Locate and identify every blood parasite.
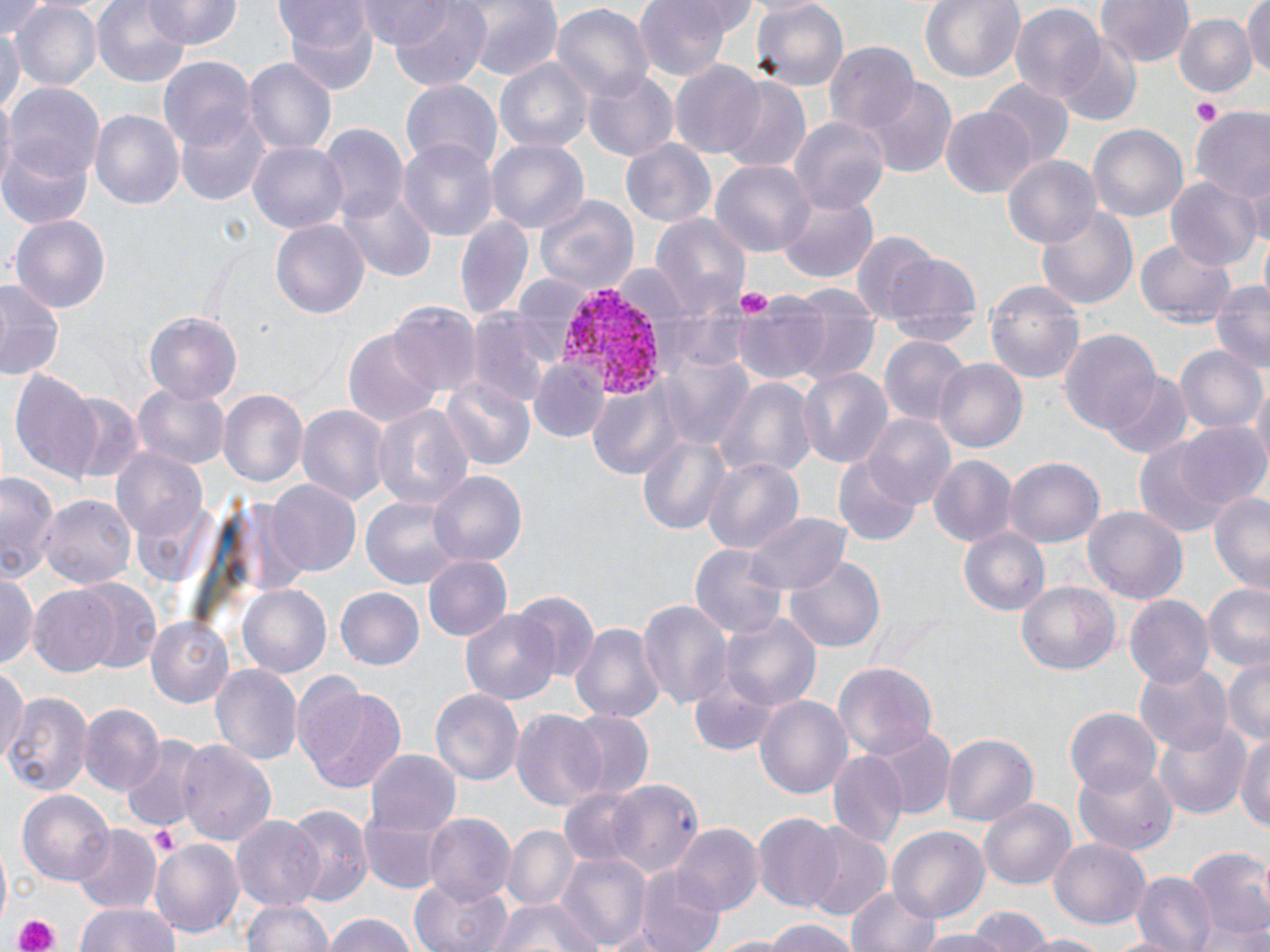

Approximate bounding boxes as (x1,y1)-(x2,y2) corner pairs in pixels.
Plasmodium vivax-infected red blood cells: (559,284)-(669,401).
No Plasmodium falciparum, Plasmodium ovale, Plasmodium malariae, Babesia divergens, or Trypanosoma brucei observed.

slide-level diagnosis = Plasmodium vivax
field of view = single
image size = 1270×952 pixels
magnification = 1000x
preparation = thin blood film
uninfected red blood cell locations = approximate bounding boxes as (x1,y1)-(x2,y2) corner pairs in pixels: (93,0)-(193,87), (144,0)-(241,47), (355,0)-(466,47), (386,0)-(493,90), (461,0)-(562,82), (636,0)-(734,80), (748,0)-(849,90), (921,0)-(1025,84), (1095,0)-(1195,68), (280,1)-(379,96), (0,2)-(51,46), (10,2)-(102,91), (550,3)-(653,104), (1242,3)-(1269,79), (1009,5)-(1105,106), (1173,13)-(1256,100), (0,21)-(22,126), (1062,40)-(1139,123), (826,43)-(918,134), (160,56)-(252,151), (245,58)-(337,158), (495,58)-(592,156), (670,60)-(767,160), (583,69)-(679,161), (721,77)-(811,173), (400,79)-(502,174), (984,79)-(1072,167), (864,80)-(957,178), (5,84)-(105,189), (174,105)-(271,206), (941,105)-(1037,199), (1190,107)-(1270,207), (90,110)-(183,210), (789,117)-(889,216), (1087,121)-(1188,222), (319,126)-(408,221), (399,137)-(499,242), (485,137)-(590,236), (620,137)-(721,228), (250,140)-(346,233), (0,141)-(95,230), (1002,155)-(1101,251), (710,160)-(812,258), (1165,175)-(1262,271), (339,188)-(436,283), (775,193)-(880,284), (532,194)-(640,296), (1034,205)-(1139,312), (648,210)-(751,316), (10,214)-(112,315), (455,214)-(533,321), (270,217)-(370,320), (0,223)-(80,365), (852,234)-(938,325), (1136,236)-(1237,328), (883,253)-(981,347), (1209,279)-(1270,375), (0,281)-(63,380), (986,282)-(1084,383), (786,287)-(879,385), (731,295)-(828,384), (388,301)-(481,398), (469,310)-(559,409), (145,313)-(242,408), (1057,324)-(1163,439), (344,327)-(441,430), (880,335)-(971,426), (1176,346)-(1267,438), (660,353)-(754,449), (530,359)-(607,441), (933,359)-(1028,455), (796,366)-(893,471), (9,370)-(105,483), (1101,373)-(1193,459), (714,376)-(816,481), (441,377)-(535,472), (1251,377)-(1270,475), (585,382)-(682,478), (134,383)-(229,470), (217,390)-(306,490), (58,392)-(147,486), (371,403)-(471,514), (297,405)-(390,510), (866,413)-(958,507), (1173,420)-(1268,511), (639,435)-(732,537), (1129,435)-(1242,539), (109,447)-(209,549), (928,454)-(1018,547), (700,455)-(804,558), (835,455)-(923,547), (1006,457)-(1102,548), (429,471)-(527,568), (1,475)-(59,585), (264,479)-(361,577), (1208,491)-(1270,595), (38,494)-(134,589), (361,496)-(468,592), (1083,502)-(1187,603), (742,512)-(852,594), (959,524)-(1051,616), (689,544)-(786,641), (421,555)-(513,643), (785,556)-(885,654), (0,571)-(40,671), (70,578)-(166,674), (1020,581)-(1121,675), (237,583)-(334,679), (1203,583)-(1270,674), (26,585)-(124,679), (334,587)-(426,671), (510,588)-(600,681), (1123,595)-(1213,690), (638,599)-(731,709), (460,608)-(559,705), (722,613)-(820,712), (144,615)-(236,707), (572,621)-(664,725), (1223,658)-(1269,745), (1134,660)-(1232,757), (832,662)-(937,763), (0,663)-(28,761), (212,666)-(301,764), (299,682)-(409,794), (430,686)-(525,786), (4,691)-(94,795), (754,691)-(852,799), (78,702)-(163,796), (1065,707)-(1163,796), (510,708)-(606,811), (564,710)-(655,800), (1152,719)-(1253,818), (869,726)-(956,820), (1234,729)-(1269,832), (940,732)-(1038,829), (120,736)-(207,833), (178,738)-(275,847), (367,748)-(460,835), (827,752)-(907,852), (1071,760)-(1176,856), (602,778)-(704,878), (559,787)-(641,868), (17,788)-(113,886), (981,799)-(1074,889), (284,804)-(372,905), (358,810)-(450,896), (422,811)-(514,907), (751,814)-(847,912), (231,816)-(325,914), (72,825)-(160,916), (501,825)-(579,912), (673,825)-(763,916), (889,828)-(988,921), (800,829)-(892,923), (150,836)-(245,935), (1050,839)-(1150,928), (1185,847)-(1270,948), (556,851)-(649,949), (636,868)-(723,952), (1133,872)-(1216,952), (411,878)-(511,952), (847,884)-(942,952), (490,896)-(600,952), (243,897)-(337,952), (72,900)-(183,952), (971,906)-(1051,952), (320,913)-(421,952), (754,918)-(859,952), (911,929)-(1018,952), (1021,933)-(1109,952)
platelet locations = approximate bounding boxes as (x1,y1)-(x2,y2) corner pairs in pixels: (1194,99)-(1220,127), (735,289)-(771,315), (151,828)-(180,858), (11,914)-(62,952)
stain = May-Grünwald-Giemsa
modality = optical microscopy